State the preparation type.
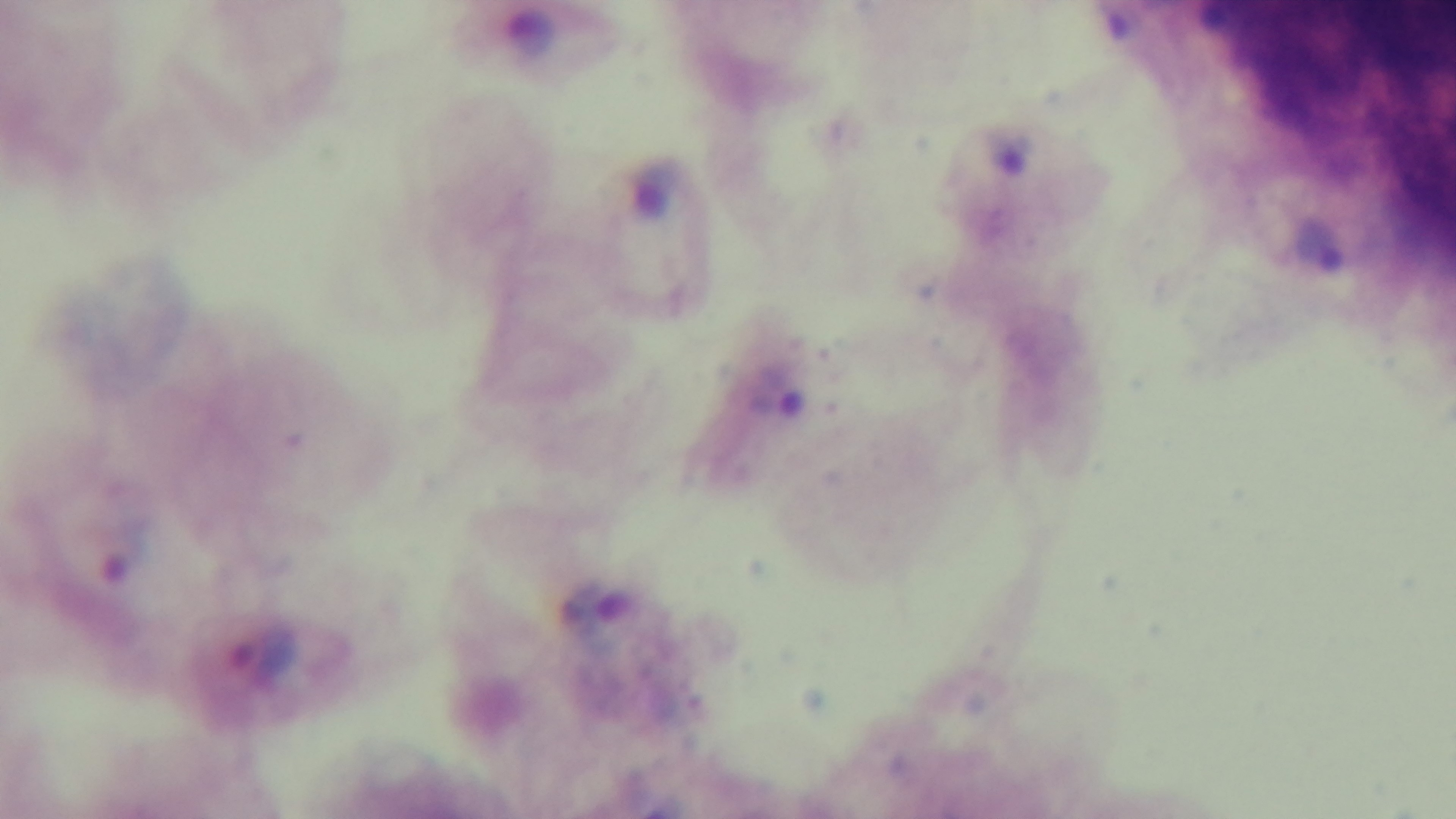
Thick.

Photomicrograph. One field from the slide. Oil-immersion objective, 100x. Mounted 4K digital camera. Malaria status: infected. Giemsa stain.